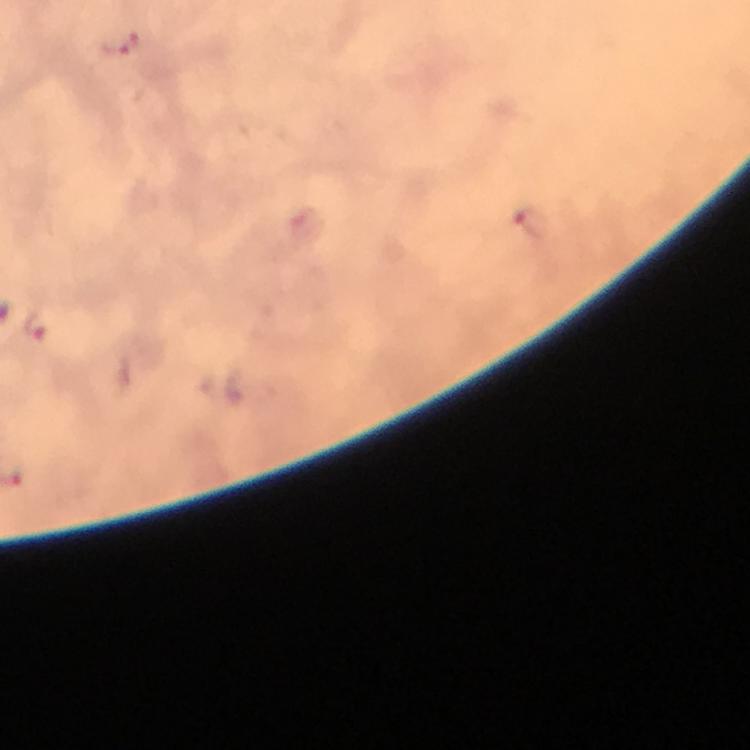
image size = 750×750 pixels
context = from a malaria diagnostic workup
preparation = thick blood film
magnification = 100x
malaria parasite locations = approximate object centers, in pixels from the top-left corner: (x=120, y=43), (x=531, y=222), (x=305, y=225), (x=36, y=325), (x=233, y=386)
capture = smartphone photograph through a microscope
immersion oil = applied
stain = Giemsa
cropped from = a single field of view